Identify the parasite.
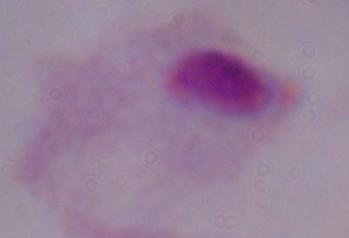

This is a trichomonad.

magnification = 1000x
modality = photomicrograph